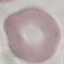
malaria_status: uninfected
capture: smartphone camera at the microscope eyepiece
image_type: automatically extracted cell patch, resized to 64 × 64 pixels
preparation: thin blood smear
stain: Giemsa